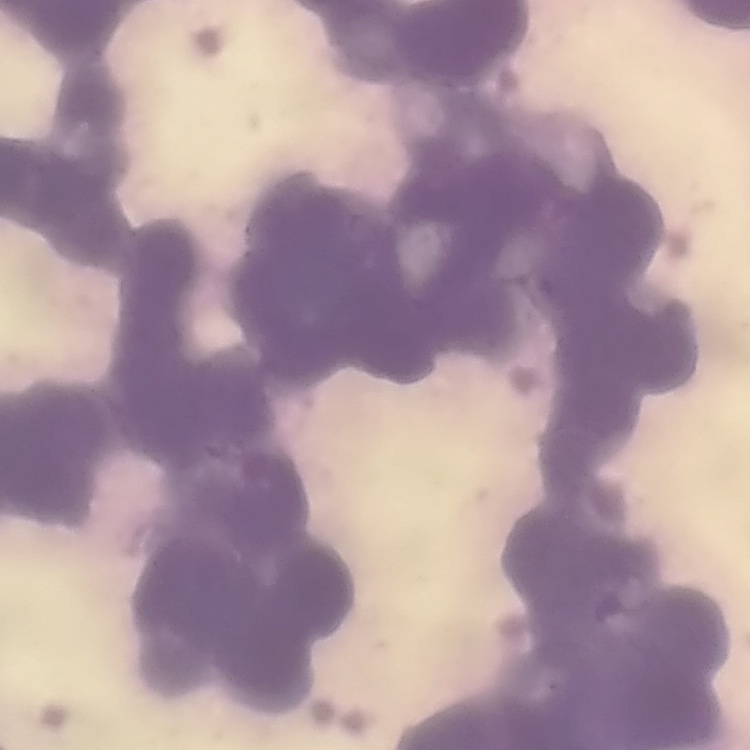 The red blood cells show rouleaux formation. Thin blood smear. Square crop of a larger photomicrograph. Field's or Giemsa stain.